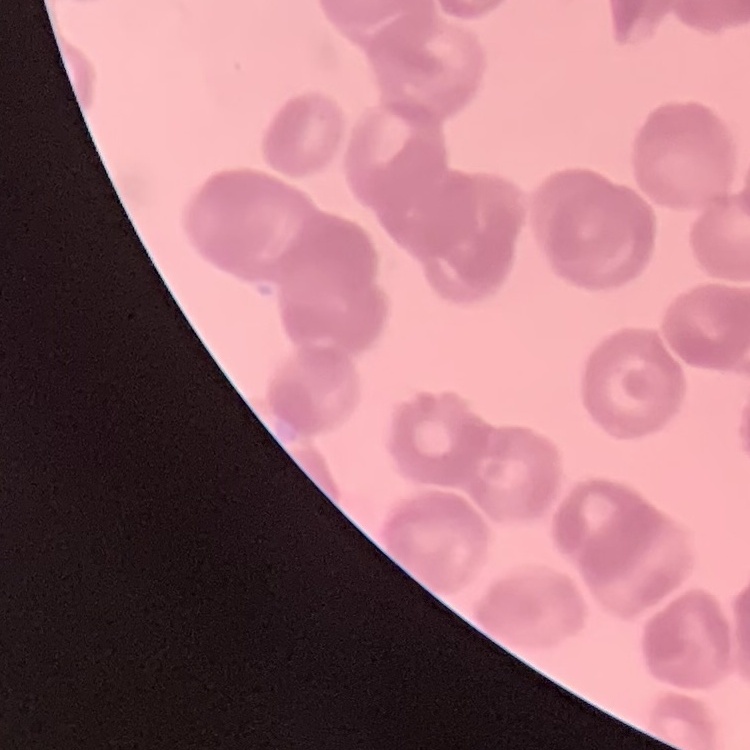 The erythrocytes show rouleaux formation. Thin blood film. One tile cut from a larger photomicrograph. Stained with either Field's or Giemsa.